Give the location of every parasitized RBC.
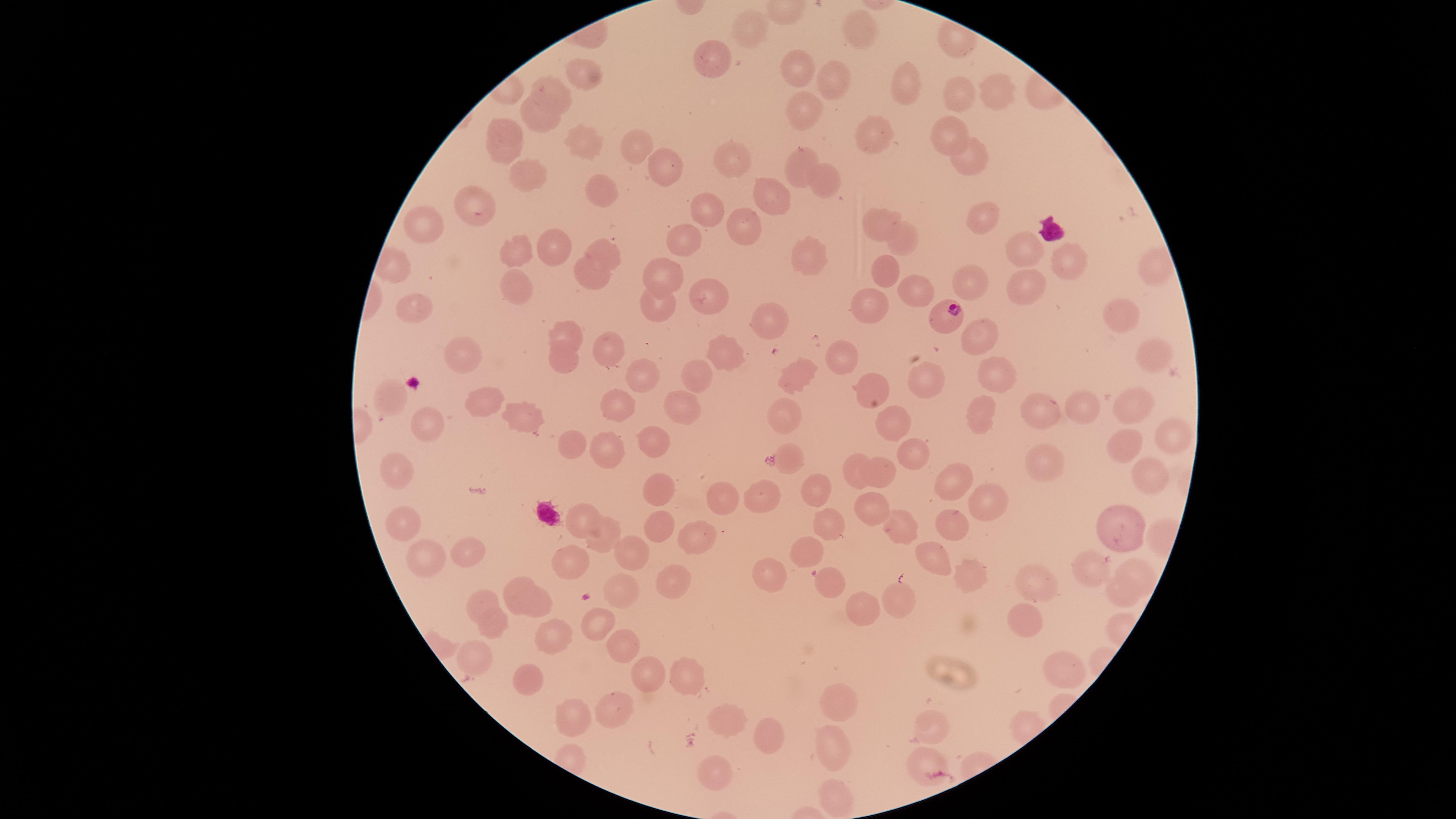
Approximate marker points as {x, y} in pixels.
Parasitized RBCs: {944, 314}.

Approximate marker points as {x, y} in pixels.
Summary:
  - Uninfected RBCs: {752, 32}, {859, 34}, {709, 69}, {793, 71}, {585, 75}, {838, 79}, {1003, 83}, {910, 88}, {555, 93}, {960, 95}, {807, 106}, {538, 121}, {952, 133}, {876, 137}, {506, 138}, {578, 140}, {636, 142}, {968, 154}, {798, 157}, {733, 159}, {661, 164}, {528, 180}, {828, 181}, {600, 189}, {769, 200}, {478, 204}, {707, 207}, {981, 217}, {874, 223}, {740, 225}, {419, 235}, {900, 239}, {691, 241}, {547, 243}, {516, 251}, {1020, 252}, {801, 255}, {609, 258}, {1064, 261}, {1148, 262}, {589, 271}, {665, 271}, {882, 271}, {966, 281}, {1021, 284}, {515, 286}, {705, 294}, {916, 295}, {655, 301}, {873, 306}, {411, 313}, {1115, 314}, {772, 320}, {563, 329}, {979, 336}, {607, 344}, {465, 348}, {841, 350}, {729, 354}, {566, 355}, {1152, 356}, {702, 373}, {641, 374}, {794, 375}, {999, 376}, {920, 378}, {871, 386}, {397, 392}, {477, 398}, {1129, 401}, {612, 403}, {680, 408}, {1073, 409}, {980, 411}, {1038, 413}, {524, 414}, {785, 419}, {889, 419}, {426, 424}, {1171, 435}, {572, 441}, {911, 445}, {647, 447}, {1122, 448}, {605, 451}, {399, 459}, {792, 459}, {1044, 460}, {851, 466}, {879, 473}, {1149, 480}, {960, 483}, {810, 489}, {655, 493}, {723, 502}, {769, 502}, {985, 502}, {869, 503}, {585, 512}, {408, 520}, {829, 522}, {902, 523}, {1122, 523}, {656, 524}, {950, 527}, {699, 533}, {604, 539}, {806, 546}, {470, 547}, {631, 547}, {936, 556}, {426, 559}, {1139, 564}, {568, 566}, {1096, 566}, {774, 572}, {821, 576}, {518, 580}, {1042, 580}, {669, 581}, {967, 581}, {620, 588}, {907, 600}, {1117, 600}, {485, 601}, {536, 605}, {869, 610}, {1024, 620}, {596, 621}, {495, 624}, {552, 634}, {623, 641}, {477, 655}, {1064, 669}, {652, 672}, {689, 675}, {529, 678}, {613, 703}, {839, 704}, {725, 719}, {577, 720}, {934, 729}, {768, 733}, {837, 747}, {920, 762}, {712, 774}, {835, 793}
  - Preparation: thin blood film
  - Image size: 1456×819 pixels
  - Stain: Giemsa
  - Field of view: single
  - Capture: smartphone photograph through the microscope eyepiece
  - Visible region: circular
  - Species: Plasmodium falciparum